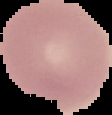

{
  "malaria_status": "uninfected",
  "image_size": "112×115 pixels",
  "image_type": "segmented cell region with the area outside set to black",
  "preparation": "thin blood smear"
}